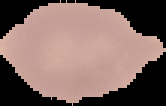
preparation: thin blood film
result: no Plasmodium parasites detected
image_size: 166×106 pixels
image_type: segmented cell region with the area outside set to black